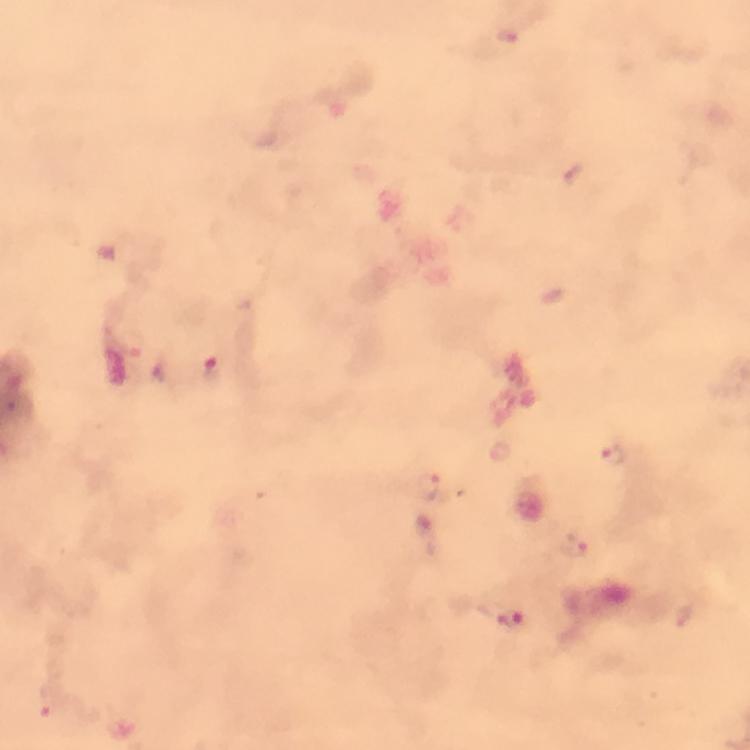

Approximate object centers, in pixels from the top-left corner. Malaria parasite locations: (x=505, y=37), (x=211, y=368), (x=612, y=456), (x=434, y=486), (x=426, y=533), (x=574, y=548), (x=510, y=620), (x=54, y=705). Immersion oil was used. Thick blood smear. 100x magnification. Smartphone photograph taken through a microscope. Image is 750×750 pixels. Giemsa-stained preparation. From a malaria diagnostic workup. Cropped region of a single field of view.